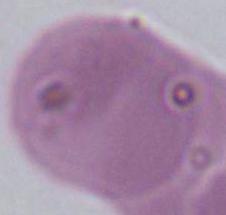
Summary:
  - Identification: red blood cell
  - Magnification: 1000x
  - Modality: photomicrograph